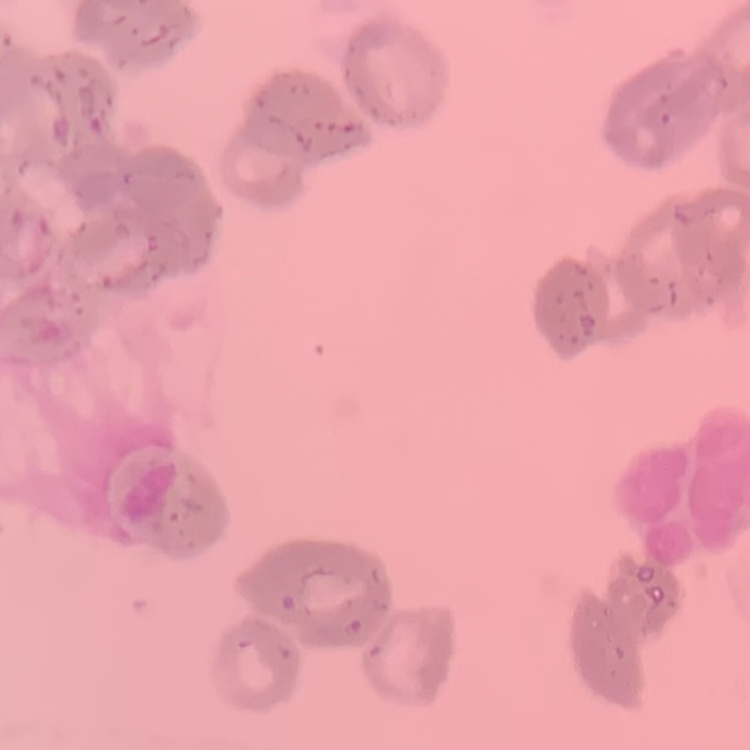 The erythrocytes exhibit rouleaux formation. Thin blood film. Field's or Giemsa stain. One tile cut from a larger photomicrograph.